Assess this cell for malaria.
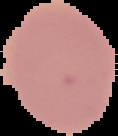
It is uninfected.

{
  "preparation": "thin blood film",
  "image_type": "segmented cell region on a black background",
  "image_size": "118×136 pixels"
}